Locate every blood parasite and identify its species.
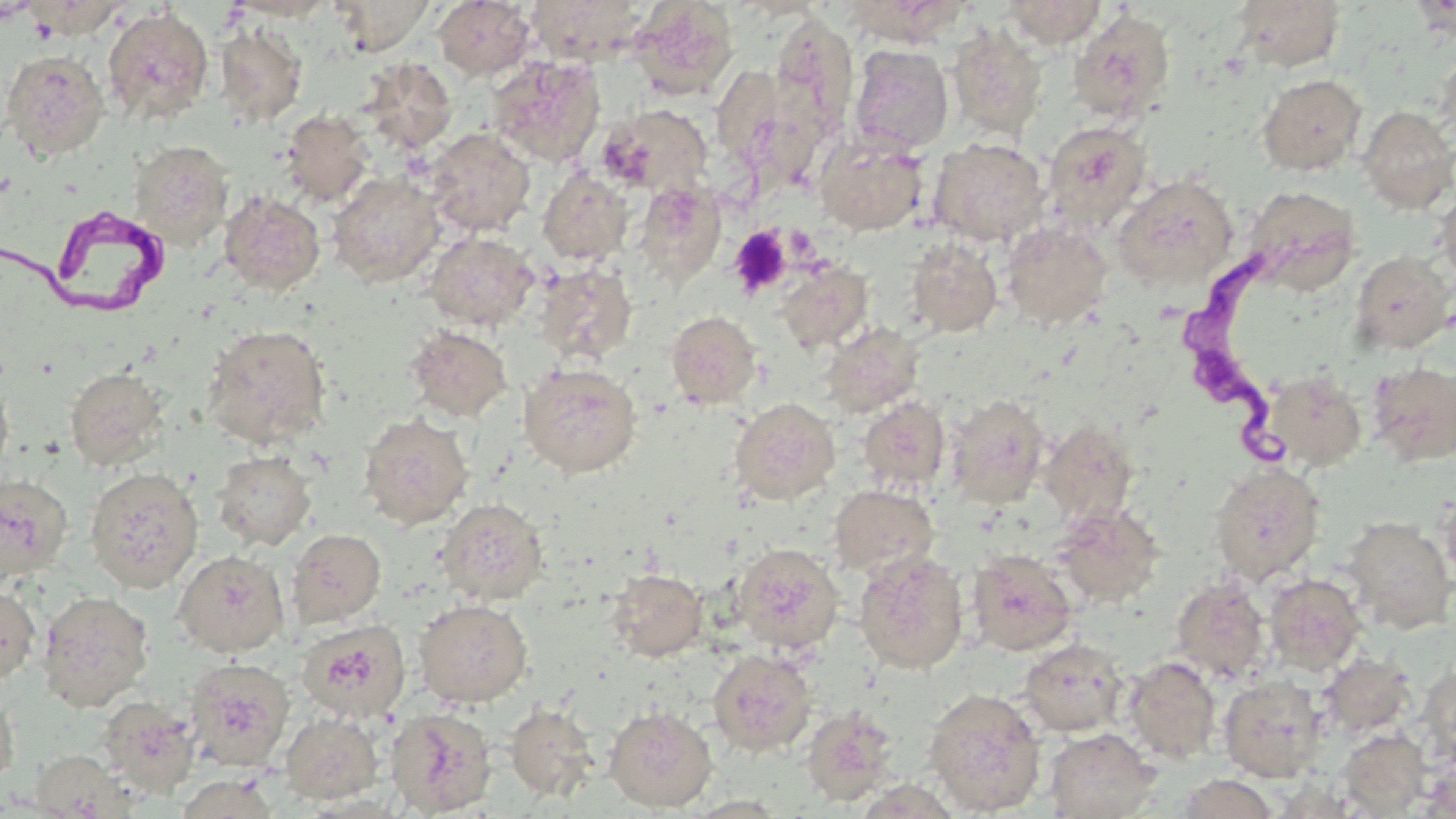

Approximate bounding boxes as [x1, y1, x2, y2] in pixels.
Trypanosoma brucei: [0, 198, 186, 322], [1180, 244, 1299, 473].
No Plasmodium falciparum, Plasmodium ovale, Plasmodium malariae, Plasmodium vivax, or Babesia divergens observed.

{
  "slide_level_diagnosis": "Trypanosoma brucei",
  "platelet_locations": "approximate bounding boxes as [x1, y1, x2, y2] in pixels: [729, 226, 792, 298]",
  "modality": "optical microscopy",
  "image_size": "1456×819 pixels",
  "field_of_view": "one of a larger specimen",
  "preparation": "thin blood smear",
  "uninfected_red_blood_cell_locations": "approximate bounding boxes as [x1, y1, x2, y2] in pixels: [224, 0, 341, 21], [329, 0, 436, 55], [526, 0, 649, 66], [1003, 0, 1106, 48], [1232, 0, 1346, 71], [433, 1, 535, 80], [629, 2, 739, 99], [102, 5, 214, 126], [1068, 9, 1176, 122], [770, 13, 858, 135], [215, 23, 308, 126], [948, 25, 1047, 140], [849, 45, 953, 155], [1436, 47, 1456, 145], [1, 50, 109, 161], [487, 55, 606, 168], [359, 58, 458, 155], [1257, 73, 1367, 176], [598, 104, 713, 197], [1357, 106, 1456, 214], [280, 110, 375, 206], [1041, 121, 1152, 233], [424, 127, 535, 237], [814, 133, 929, 236], [929, 138, 1049, 247], [130, 140, 234, 249], [538, 169, 633, 265], [327, 172, 445, 288], [1113, 173, 1240, 291], [633, 182, 726, 286], [1243, 185, 1363, 294], [1435, 188, 1456, 285], [219, 191, 325, 296], [1001, 222, 1113, 332], [424, 231, 539, 331], [904, 238, 1003, 338], [1351, 251, 1454, 355], [777, 262, 873, 354], [535, 263, 637, 364], [666, 311, 761, 409], [818, 321, 924, 418], [201, 324, 332, 449], [405, 326, 512, 422], [1367, 361, 1456, 466], [519, 363, 642, 477], [65, 366, 168, 469], [1261, 371, 1367, 471], [0, 377, 15, 483], [945, 393, 1050, 509], [731, 397, 840, 505], [859, 397, 951, 493], [358, 413, 473, 529], [1039, 420, 1138, 527], [213, 451, 316, 551], [1209, 462, 1325, 584], [85, 466, 203, 592], [0, 473, 73, 584], [829, 484, 939, 577], [1439, 490, 1456, 591], [437, 499, 548, 605], [1052, 505, 1164, 608], [1341, 516, 1455, 633], [287, 528, 386, 628], [732, 543, 843, 654], [967, 549, 1078, 656], [174, 550, 289, 656], [854, 551, 968, 674], [606, 569, 708, 661], [1264, 573, 1366, 674], [1169, 576, 1270, 682], [0, 585, 40, 683], [38, 591, 154, 710], [414, 599, 533, 707], [296, 619, 410, 723], [286, 620, 390, 806], [1018, 638, 1128, 737], [708, 648, 817, 757], [1320, 653, 1416, 737], [1123, 656, 1222, 763], [184, 657, 295, 771], [1418, 661, 1456, 766], [1219, 675, 1327, 782], [0, 683, 19, 793], [923, 687, 1046, 815], [98, 697, 200, 797], [505, 703, 599, 802], [604, 705, 717, 812], [801, 705, 899, 806], [385, 707, 497, 817], [279, 712, 383, 805], [1044, 728, 1162, 818], [1338, 729, 1431, 816], [29, 752, 134, 817], [1423, 757, 1456, 818], [173, 773, 280, 818], [1175, 774, 1279, 818]",
  "magnification": "1000x",
  "stain": "May-Grünwald-Giemsa"
}